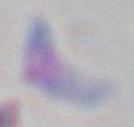

{
  "identification": "Toxoplasma gondii",
  "magnification": "1000x",
  "modality": "micrograph"
}